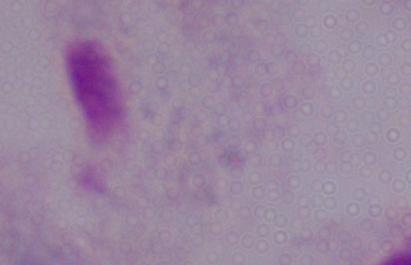

1000x magnification. A trichomonad is shown. Micrograph.